Assess this cell for malaria.
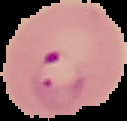
Parasitized.

Summary:
  - Image size: 127×121 pixels
  - Image type: cell region segmented out of the field of view; surrounding area masked to black
  - Preparation: thin blood smear